State which parasite is depicted.
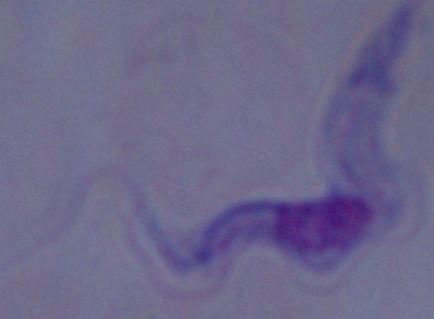
This is a trypanosome.

Photomicrograph. Captured at 1000x magnification.